Assess the morphology of the erythrocytes.
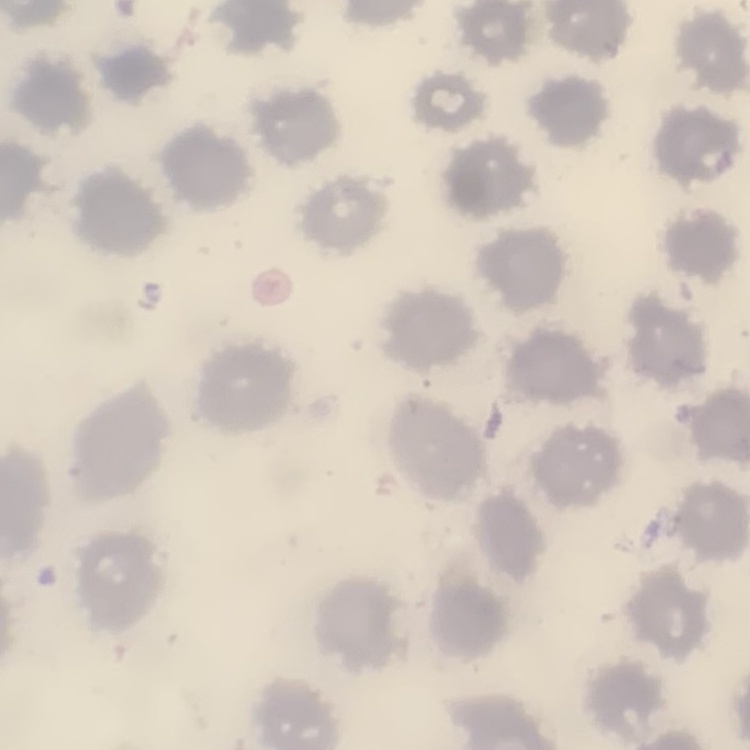
No rouleaux formation.

Summary:
  - Image type: one tile cut from a larger photomicrograph
  - Preparation: thin peripheral smear
  - Stain: Field's or Giemsa